Name the parasite shown.
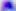
Toxoplasma gondii.

Summary:
  - Modality: photomicrograph
  - Magnification: 400x